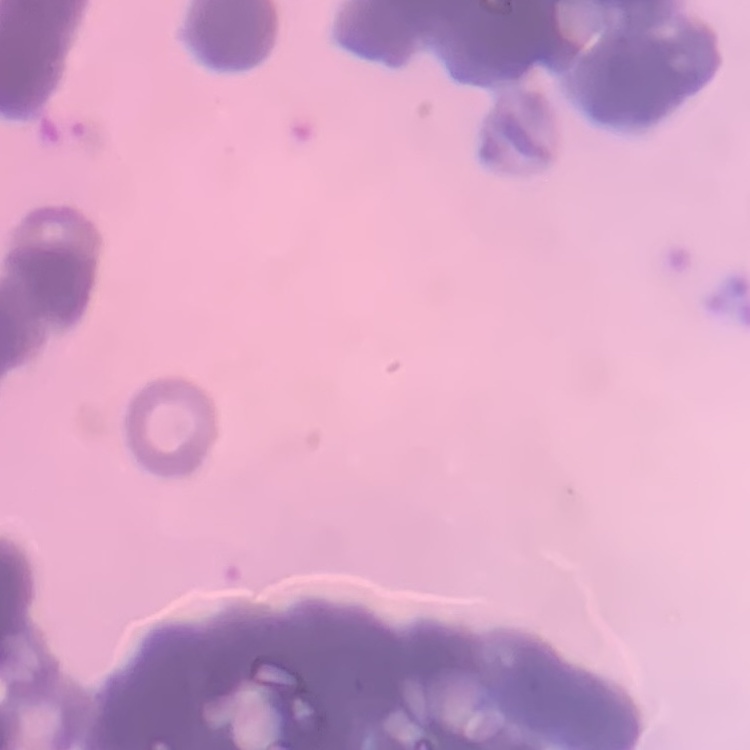
red blood cell morphology = rouleaux formation
stain = Field's or Giemsa
preparation = thin peripheral smear
image type = square crop of a larger photomicrograph